Identify the parasite.
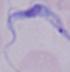
This is a trypanosome.

Summary:
  - Magnification: 1000x
  - Modality: photomicrograph